Assess this cell for malaria.
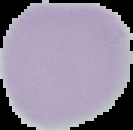

It is uninfected.

Summary:
  - Image type: segmented cell region with the area outside set to black
  - Image size: 133×130 pixels
  - Preparation: thin blood smear